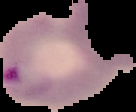

From a thin blood smear. Image is 136×112 pixels. The area outside the segmented cell region is set to black. Malaria status: parasitized.